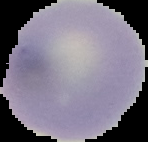
image_type: segmented cell region with the area outside set to black
preparation: thin blood smear
malaria_status: uninfected
image_size: 148×142 pixels